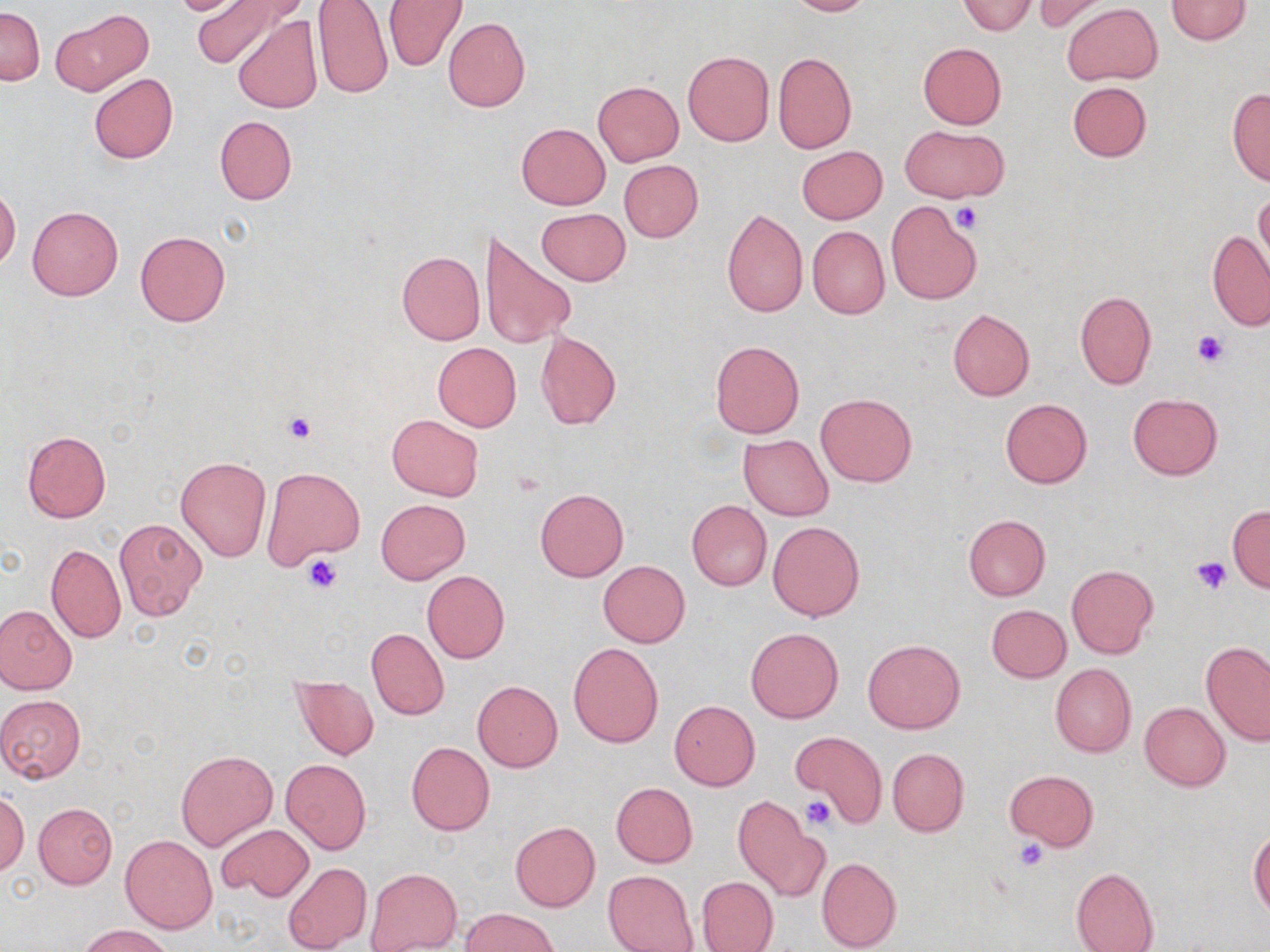

Approximate bounding boxes as (x1,y1)-(x2,y2) corner pairs in pixels. Platelet locations: (954,204)-(983,232), (1193,330)-(1227,368), (282,411)-(317,444), (302,554)-(342,594), (1189,555)-(1231,595), (801,797)-(834,828), (1013,838)-(1049,872). Uninfected red blood cell locations: (162,0)-(258,16), (191,0)-(294,70), (382,0)-(467,72), (785,0)-(872,16), (1031,0)-(1112,34), (1166,0)-(1253,43), (958,1)-(1036,34), (312,2)-(393,100), (1061,3)-(1162,86), (0,6)-(44,85), (387,7)-(524,92), (50,8)-(154,96), (232,15)-(324,114), (443,17)-(530,112), (917,42)-(1006,129), (682,50)-(775,147), (773,52)-(856,153), (88,73)-(178,163), (593,81)-(684,165), (1067,82)-(1152,162), (1226,87)-(1270,185), (215,116)-(297,204), (515,123)-(610,209), (899,125)-(1009,203), (796,146)-(888,225), (619,159)-(703,242), (1255,188)-(1270,273), (0,189)-(20,269), (886,201)-(981,304), (27,206)-(123,300), (721,207)-(808,318), (536,208)-(630,286), (479,226)-(577,351), (807,226)-(889,320), (135,230)-(231,327), (1208,230)-(1270,332), (396,251)-(485,344), (1075,290)-(1156,389), (947,308)-(1035,400), (535,331)-(621,429), (709,340)-(805,439), (433,342)-(522,432), (816,393)-(916,486), (1127,394)-(1222,480), (999,398)-(1093,488), (386,414)-(483,501), (22,431)-(111,522), (739,435)-(835,521), (176,456)-(271,561), (262,466)-(364,570), (535,488)-(628,581), (377,499)-(469,583), (687,500)-(771,591), (1227,504)-(1270,593), (962,514)-(1050,602), (114,517)-(207,622), (768,521)-(864,621), (45,543)-(126,643), (598,561)-(691,647), (1067,565)-(1158,660), (421,570)-(509,664), (0,604)-(77,695), (986,604)-(1071,682), (746,627)-(843,724), (366,628)-(449,719), (864,639)-(965,733), (1202,641)-(1270,745), (568,643)-(663,747), (1049,663)-(1137,757), (292,675)-(378,761), (473,681)-(563,771), (0,694)-(87,782), (670,700)-(760,790), (1140,702)-(1230,791), (794,731)-(886,827), (406,742)-(495,835), (887,748)-(969,836), (176,749)-(279,852), (280,759)-(371,854), (1005,770)-(1098,851), (611,783)-(698,867), (0,792)-(29,875), (731,798)-(826,902), (33,802)-(117,888), (509,821)-(601,912), (216,824)-(314,901), (1249,828)-(1270,916), (121,835)-(217,933), (816,857)-(901,951), (282,862)-(373,952), (1072,867)-(1159,952), (365,868)-(462,951), (602,870)-(698,952), (696,876)-(777,951), (461,909)-(559,952), (78,923)-(176,952). Slide-level diagnosis: negative for blood parasites. Thin blood film. Light microscopy. Image is 1270×952 pixels. One field of a larger specimen. May-Grünwald-Giemsa-stained preparation. Captured at 1000x magnification.